State which parasite is depicted.
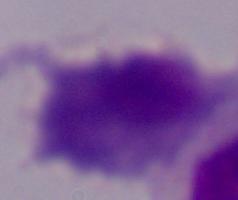
This is a trichomonad.

magnification: 1000x
modality: micrograph